Assess the morphology of the red blood cells.
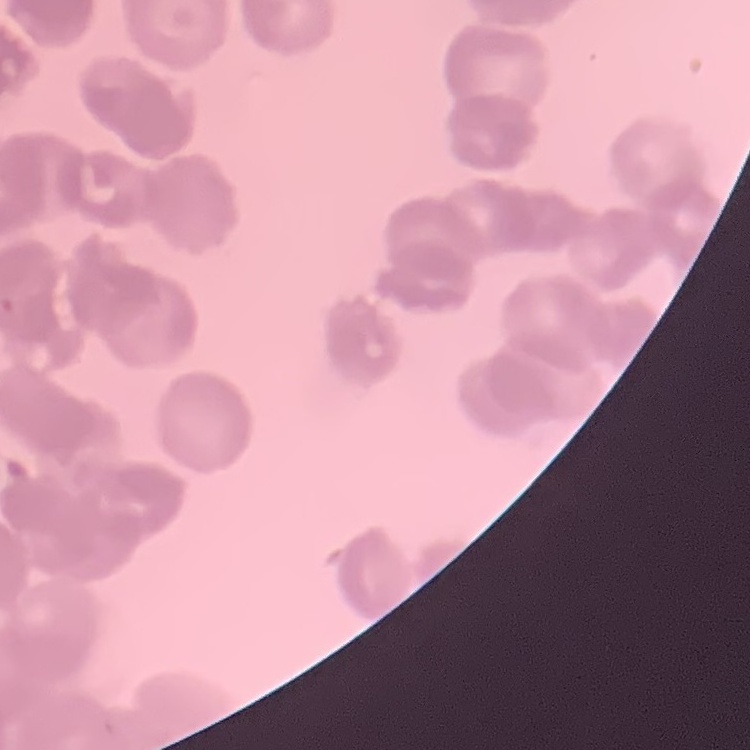
Rouleaux formation.

stain = Field's or Giemsa
image type = one tile cut from a larger photomicrograph
preparation = thin blood film